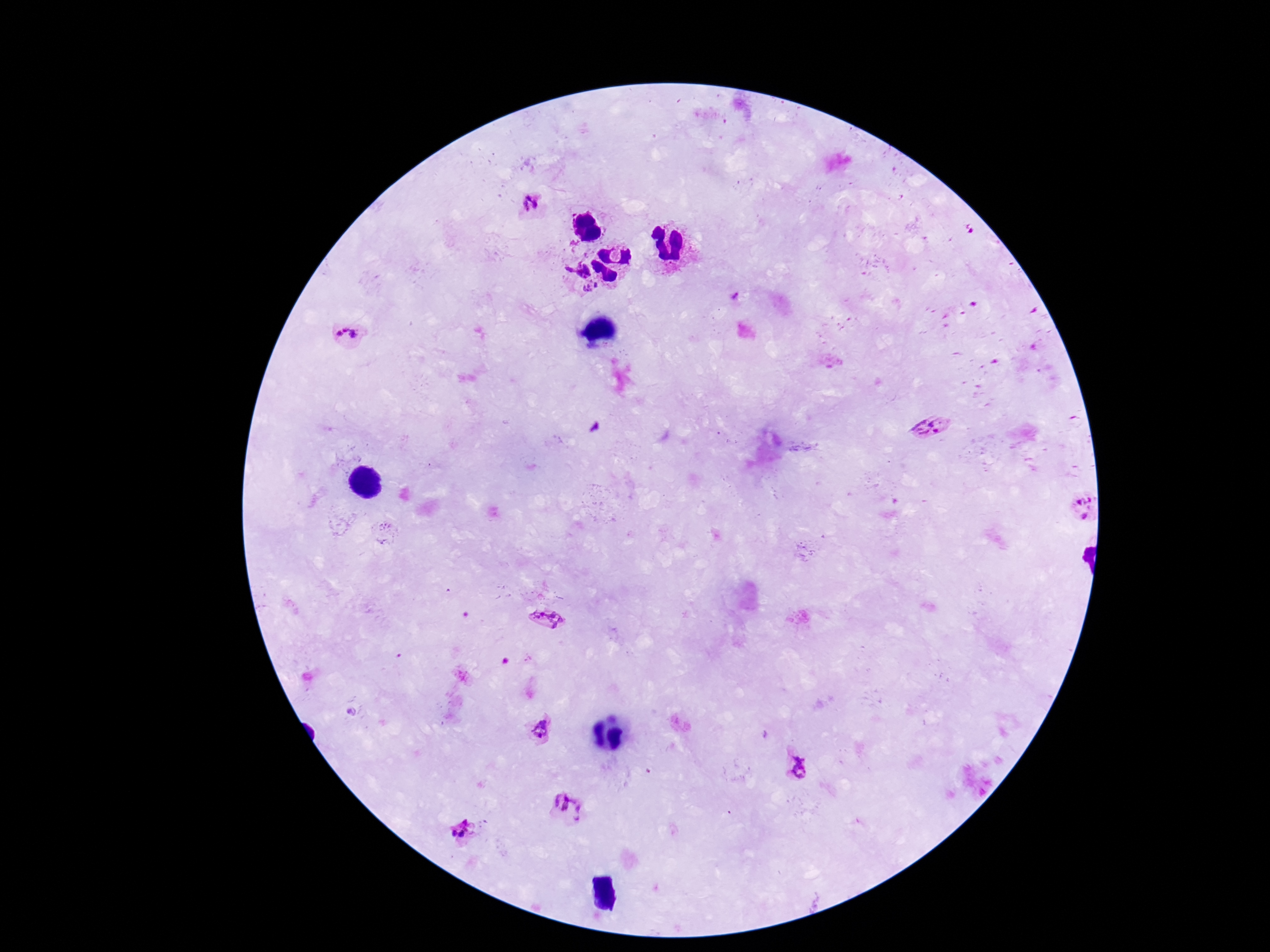
Approximate object centers, in pixels from the top-left corner.
Summary:
  - Plasmodium parasite locations: (x=531, y=205), (x=568, y=269), (x=598, y=284), (x=587, y=289), (x=348, y=334), (x=930, y=427), (x=1086, y=507), (x=549, y=620), (x=540, y=730), (x=803, y=767), (x=569, y=806), (x=464, y=831)
  - Magnification: 100x
  - Image size: 1270×952 pixels
  - Stain: Giemsa
  - Patient malaria status: infected
  - Preparation: thick peripheral-blood smear
  - Capture: smartphone camera through the microscope eyepiece
  - Field of view: one from this slide